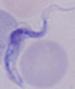

A trypanosome is shown. Micrograph. Captured at 1000x magnification.